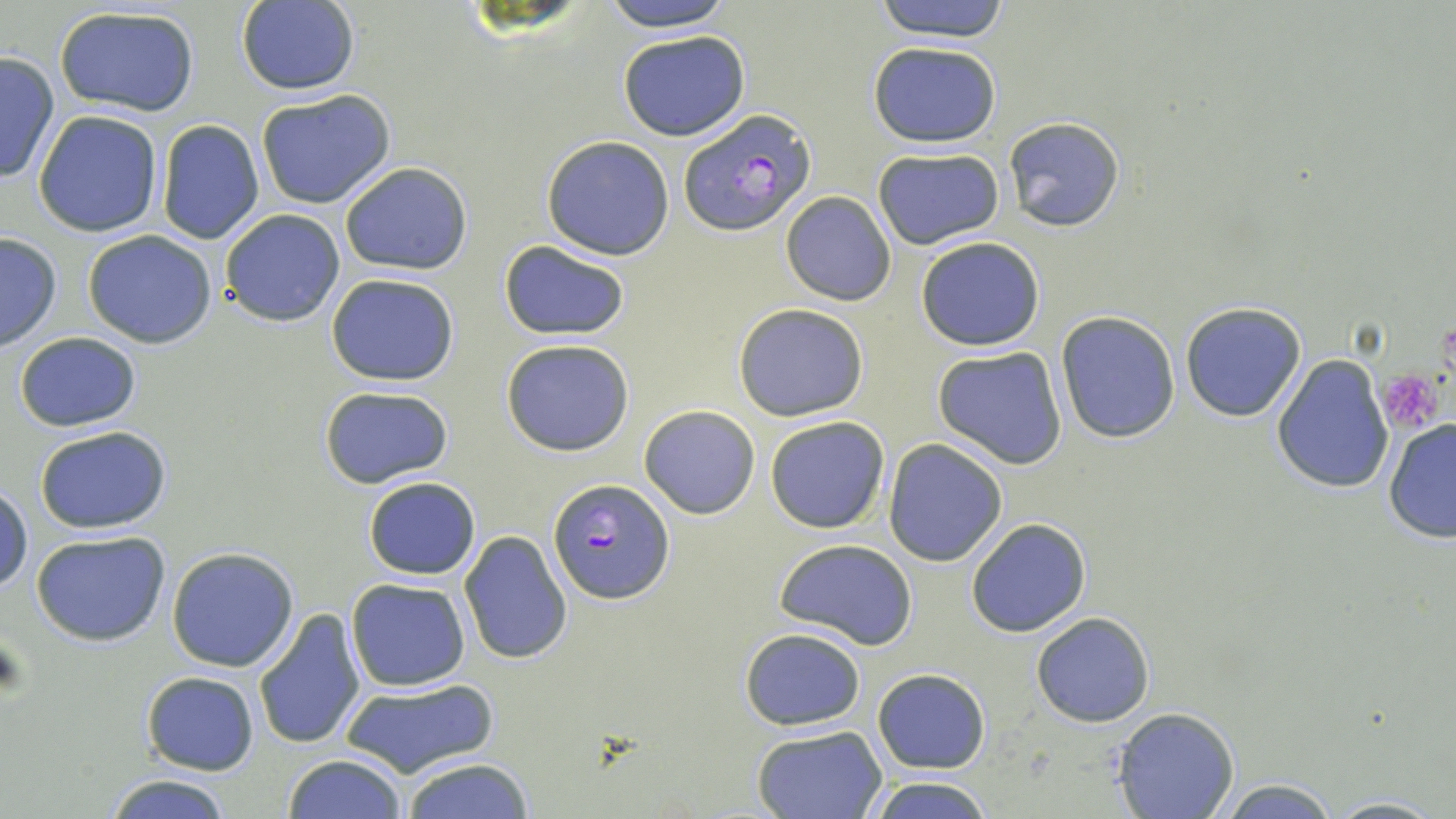
Approximate bounding boxes as named x1/y1/x2/y2 corners in pixels. Plasmodium falciparum-infected red blood cell locations: (x1=679, y1=110, x2=815, y2=236), (x1=548, y1=478, x2=674, y2=605). Platelet locations: (x1=1376, y1=370, x2=1442, y2=433). Uninfected red blood cell locations: (x1=596, y1=0, x2=737, y2=32), (x1=870, y1=0, x2=1014, y2=41), (x1=235, y1=1, x2=360, y2=96), (x1=53, y1=5, x2=202, y2=118), (x1=618, y1=30, x2=750, y2=140), (x1=868, y1=40, x2=1001, y2=148), (x1=0, y1=49, x2=60, y2=185), (x1=255, y1=90, x2=397, y2=209), (x1=33, y1=110, x2=164, y2=238), (x1=1003, y1=117, x2=1125, y2=233), (x1=155, y1=120, x2=264, y2=245), (x1=541, y1=135, x2=676, y2=260), (x1=872, y1=148, x2=1004, y2=249), (x1=338, y1=162, x2=473, y2=276), (x1=781, y1=191, x2=896, y2=306), (x1=220, y1=209, x2=346, y2=327), (x1=82, y1=229, x2=218, y2=349), (x1=0, y1=233, x2=61, y2=350), (x1=915, y1=237, x2=1045, y2=351), (x1=500, y1=241, x2=632, y2=341), (x1=326, y1=272, x2=460, y2=387), (x1=1180, y1=301, x2=1307, y2=422), (x1=733, y1=303, x2=871, y2=422), (x1=1056, y1=311, x2=1181, y2=443), (x1=12, y1=330, x2=143, y2=433), (x1=501, y1=340, x2=635, y2=456), (x1=932, y1=345, x2=1068, y2=468), (x1=1271, y1=354, x2=1394, y2=495), (x1=317, y1=385, x2=455, y2=490), (x1=638, y1=405, x2=761, y2=519), (x1=764, y1=415, x2=891, y2=534), (x1=1382, y1=421, x2=1456, y2=543), (x1=34, y1=425, x2=171, y2=532), (x1=882, y1=440, x2=1007, y2=567), (x1=363, y1=476, x2=482, y2=580), (x1=1, y1=484, x2=32, y2=596), (x1=965, y1=518, x2=1091, y2=638), (x1=30, y1=530, x2=171, y2=645), (x1=457, y1=530, x2=572, y2=665), (x1=771, y1=537, x2=922, y2=652), (x1=167, y1=547, x2=299, y2=672), (x1=346, y1=576, x2=472, y2=692), (x1=252, y1=608, x2=367, y2=751), (x1=1031, y1=612, x2=1155, y2=727), (x1=738, y1=626, x2=867, y2=731), (x1=872, y1=669, x2=990, y2=774), (x1=140, y1=671, x2=258, y2=775), (x1=337, y1=677, x2=496, y2=780), (x1=1112, y1=706, x2=1238, y2=817), (x1=751, y1=726, x2=887, y2=818), (x1=282, y1=753, x2=408, y2=819), (x1=399, y1=757, x2=535, y2=817), (x1=103, y1=774, x2=233, y2=818), (x1=867, y1=776, x2=995, y2=819), (x1=1208, y1=777, x2=1344, y2=818), (x1=1315, y1=794, x2=1449, y2=818). Slide-level diagnosis: Plasmodium falciparum. May-Grünwald-Giemsa stain. Optical microscopy. 1000x magnification. One field of a larger specimen. Thin blood film. Image is 1456×819 pixels.